Assess this cell for malaria.
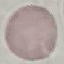
It is uninfected.

Summary:
  - Preparation: thin blood smear
  - Capture: smartphone camera at the microscope eyepiece
  - Image type: automatically extracted cell patch, resized to 64 × 64 pixels
  - Stain: Giemsa